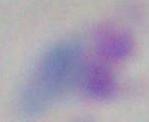

Summary:
  - Modality: micrograph
  - Magnification: 1000x
  - Identification: Toxoplasma gondii